State which cell type is depicted.
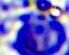
A leukocyte.

Captured at 400x magnification. Micrograph.